State which parasite is depicted.
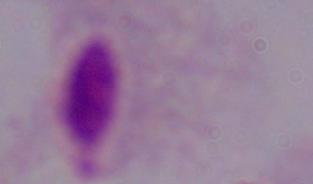
This is a trichomonad.

modality = photomicrograph
magnification = 1000x